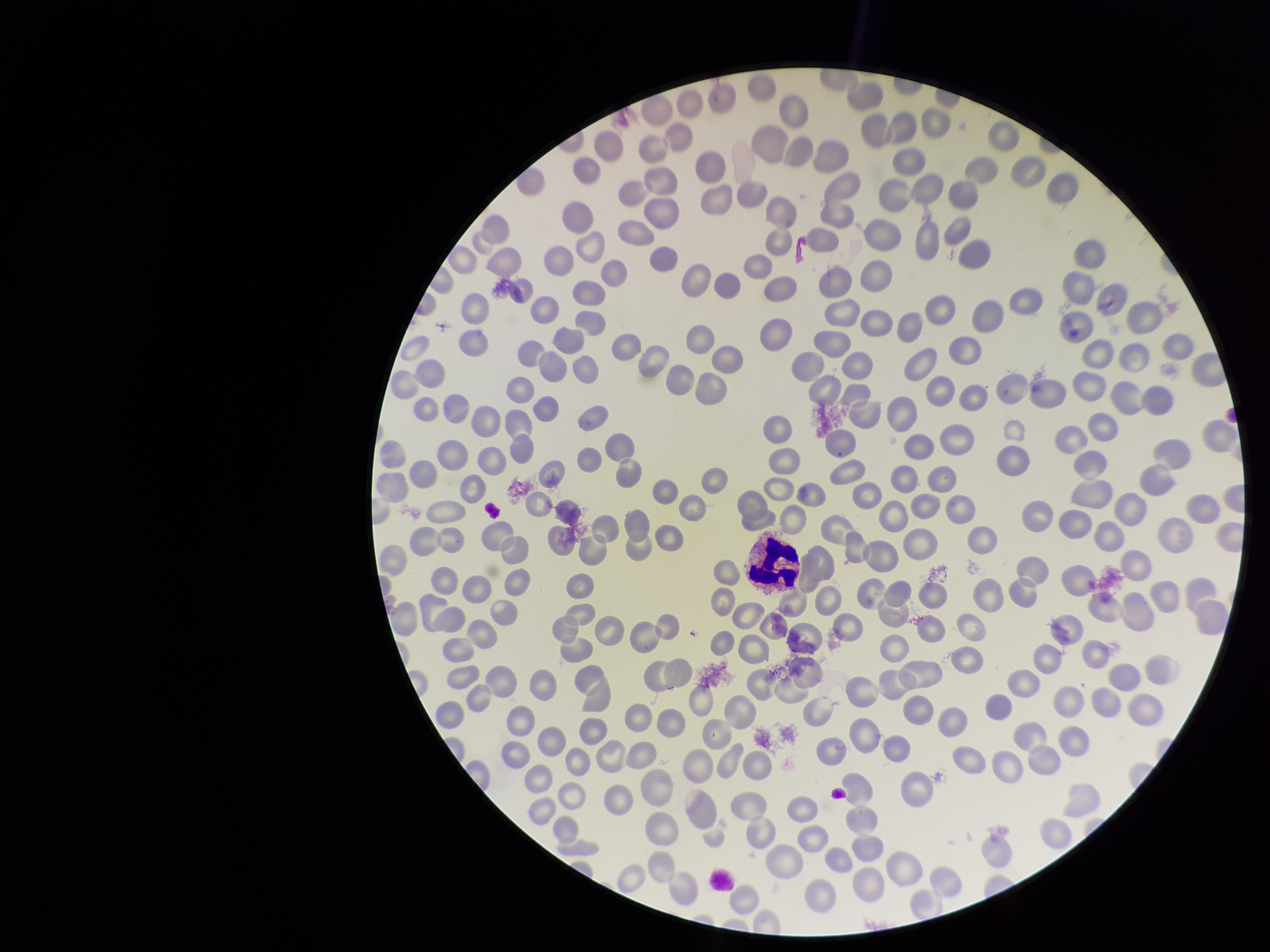
Summary:
  - Red blood cell count: 274
  - Parasitized red blood cell count: 0
  - Field of view: single
  - Patient malaria status: negative
  - Capture: smartphone photograph through the microscope eyepiece
  - Stain: Giemsa
  - Preparation: thin blood smear
  - Parasitized red blood cells: none detected
  - Image size: 1270×952 pixels